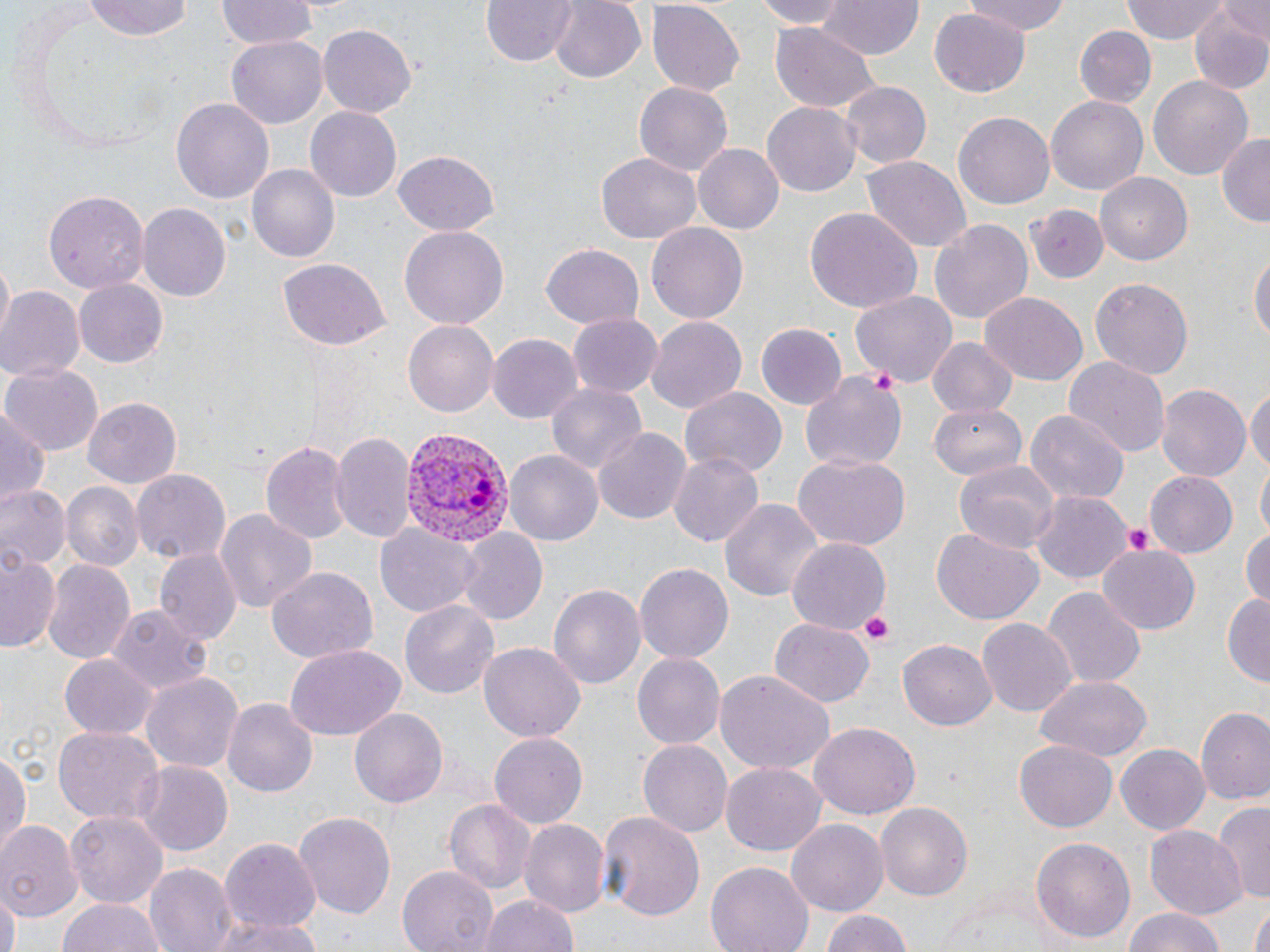

Summary:
  - Coordinate format: approximate bounding boxes as (x1,y1)-(x2,y2) corner pairs in pixels
  - Plasmodium vivax-infected red blood cell locations: (393,422)-(513,547)
  - Uninfected red blood cell locations: (85,0)-(194,42), (217,0)-(317,47), (482,0)-(578,67), (548,0)-(645,83), (746,0)-(854,27), (820,0)-(922,60), (963,0)-(1072,35), (1120,0)-(1234,42), (1189,1)-(1270,93), (646,3)-(746,95), (930,7)-(1029,96), (319,23)-(416,118), (769,24)-(881,114), (1075,26)-(1155,108), (227,33)-(327,127), (1147,72)-(1252,177), (633,82)-(733,175), (840,82)-(931,168), (1046,94)-(1149,196), (171,98)-(273,204), (763,102)-(861,195), (306,106)-(402,203), (955,113)-(1055,209), (1215,134)-(1270,225), (692,143)-(783,234), (393,150)-(501,235), (598,152)-(701,244), (862,158)-(971,252), (247,166)-(338,264), (1095,171)-(1193,265), (43,189)-(149,294), (136,201)-(229,299), (1028,203)-(1111,284), (804,205)-(921,314), (928,218)-(1035,326), (645,221)-(750,324), (399,227)-(507,331), (541,244)-(645,329), (1250,248)-(1269,352), (279,259)-(389,349), (1088,276)-(1195,380), (74,278)-(169,367), (0,287)-(83,385), (852,291)-(957,389), (981,291)-(1088,385), (567,313)-(661,398), (647,318)-(746,412), (403,320)-(498,417), (756,324)-(846,411), (487,333)-(581,426), (925,337)-(1019,419), (1064,355)-(1171,457), (5,363)-(103,454), (800,371)-(908,476), (546,380)-(647,478), (1154,383)-(1251,483), (1248,383)-(1270,482), (680,387)-(787,479), (81,395)-(183,486), (928,401)-(1029,482), (1,407)-(50,511), (1026,409)-(1125,507), (593,427)-(689,525), (330,431)-(417,546), (261,442)-(349,542), (669,449)-(766,547), (506,450)-(604,547), (792,453)-(910,553), (953,459)-(1062,554), (1256,463)-(1269,546), (133,470)-(230,566), (1146,470)-(1240,558), (60,482)-(142,572), (0,483)-(70,574), (1028,491)-(1134,585), (719,496)-(821,608), (213,509)-(317,618), (376,524)-(482,617), (1241,526)-(1269,610), (932,527)-(1045,626), (455,528)-(547,626), (787,540)-(889,632), (1098,541)-(1200,633), (0,547)-(61,656), (153,550)-(241,645), (41,558)-(135,668), (635,563)-(735,663), (267,567)-(378,663), (547,581)-(645,688), (1043,588)-(1145,688), (1223,594)-(1270,686), (400,597)-(500,696), (106,605)-(210,696), (768,619)-(875,707), (978,619)-(1077,717), (897,640)-(997,731), (479,643)-(585,743), (283,644)-(406,741), (633,652)-(725,749), (60,655)-(156,739), (715,669)-(836,774), (140,670)-(243,776), (1036,676)-(1151,761), (224,699)-(317,796), (350,707)-(448,807), (1197,709)-(1270,807), (808,723)-(918,821), (54,727)-(161,824), (489,733)-(587,828), (640,741)-(731,838), (1016,741)-(1117,831), (1116,744)-(1210,834), (0,749)-(29,860), (722,760)-(824,855), (135,761)-(232,856), (445,799)-(535,895), (1215,800)-(1270,905), (877,801)-(972,904), (68,809)-(167,906), (599,810)-(704,920), (293,811)-(398,921), (519,818)-(610,920), (787,819)-(886,918), (0,821)-(80,919), (1146,827)-(1245,916), (1030,837)-(1136,944), (220,838)-(323,933), (706,862)-(813,952), (145,864)-(235,952), (398,866)-(497,952), (0,888)-(18,952), (481,893)-(579,952), (58,896)-(163,952), (1247,906)-(1269,952), (1120,907)-(1229,952), (817,909)-(916,952), (210,915)-(318,952)
  - Platelet locations: (871,367)-(902,396), (1125,524)-(1155,555), (857,613)-(897,646)
  - Slide-level diagnosis: Plasmodium vivax
  - Modality: optical microscopy
  - Stain: May-Grünwald-Giemsa
  - Preparation: thin blood smear
  - Field of view: one of a larger specimen
  - Image size: 1270×952 pixels
  - Magnification: 1000x